Outline platelets.
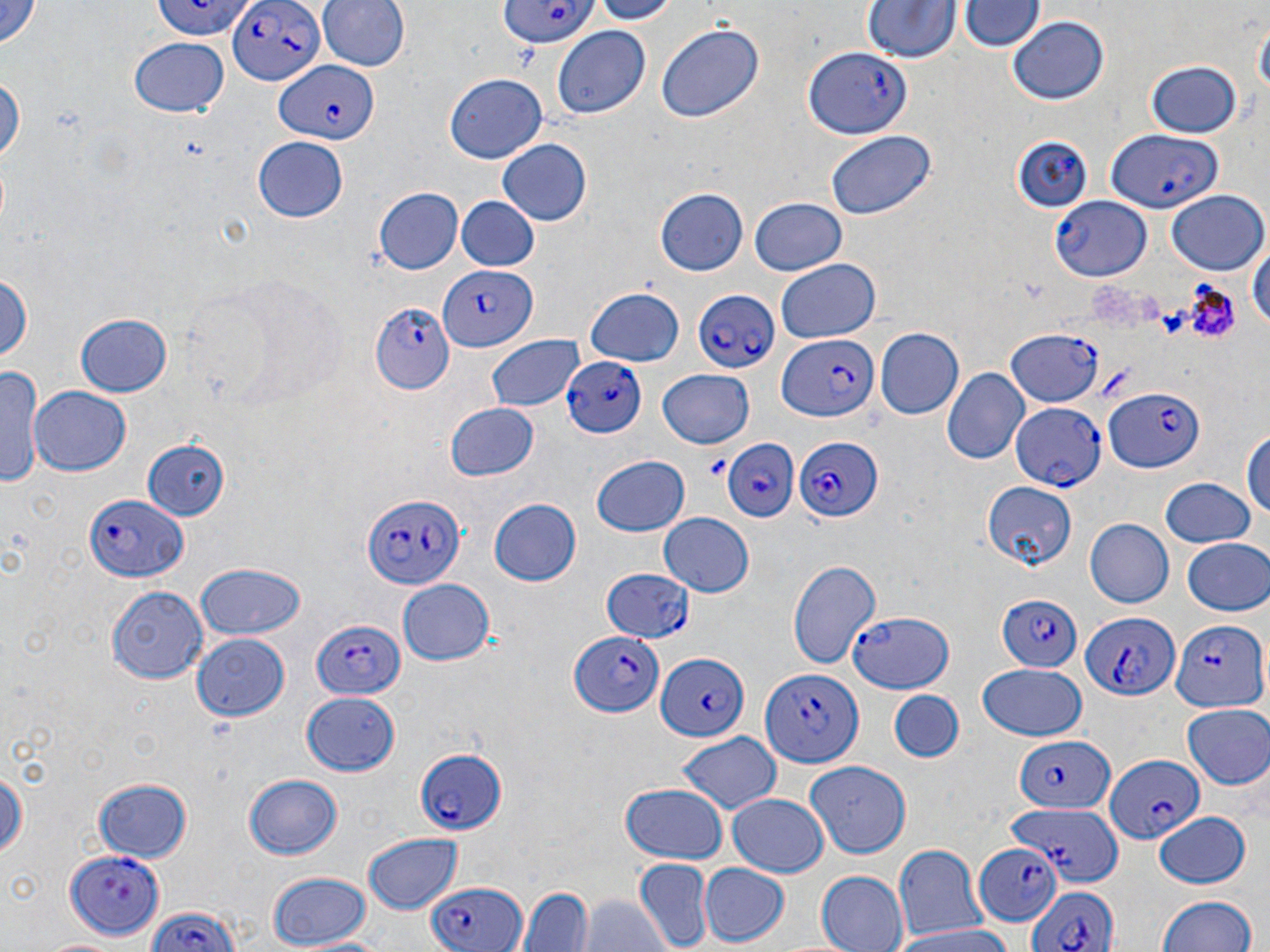
Approximate bounding boxes as [x1, y1, x2, y2] in pixels.
Platelets: [702, 452, 731, 481].

Plasmodium falciparum-infected red blood cell locations: [153, 0, 250, 40], [227, 0, 324, 88], [491, 3, 601, 47], [804, 44, 912, 140], [271, 64, 378, 147], [1108, 130, 1222, 213], [1012, 134, 1091, 214], [1052, 197, 1151, 279], [435, 266, 536, 352], [693, 287, 778, 374], [371, 300, 454, 394], [1008, 328, 1098, 408], [777, 336, 878, 423], [562, 354, 646, 438], [1102, 387, 1204, 474], [1009, 401, 1104, 491], [798, 435, 884, 522], [719, 437, 800, 524], [84, 489, 191, 583], [362, 491, 468, 590], [597, 564, 697, 649], [995, 593, 1083, 672], [849, 608, 955, 693], [1082, 613, 1180, 700], [1167, 618, 1266, 711], [309, 620, 404, 699], [571, 628, 665, 719], [653, 650, 750, 742], [756, 660, 865, 770], [1012, 736, 1115, 812], [415, 747, 508, 833], [1103, 755, 1202, 844], [1012, 795, 1124, 884], [971, 842, 1063, 924], [66, 848, 166, 936], [422, 881, 527, 952], [1027, 884, 1117, 952], [143, 908, 248, 952]. Uninfected red blood cell locations: [0, 0, 46, 46], [317, 0, 407, 74], [585, 0, 681, 24], [863, 1, 960, 64], [962, 1, 1041, 53], [1253, 12, 1268, 107], [1007, 16, 1109, 106], [656, 24, 762, 126], [550, 26, 651, 117], [130, 39, 228, 118], [1144, 61, 1243, 137], [0, 73, 24, 169], [444, 74, 548, 164], [826, 128, 934, 220], [253, 138, 349, 222], [496, 139, 592, 226], [654, 187, 749, 275], [373, 188, 463, 273], [1166, 191, 1267, 273], [455, 196, 541, 273], [747, 197, 848, 276], [1251, 231, 1269, 338], [774, 259, 882, 343], [0, 270, 33, 368], [583, 286, 686, 367], [76, 313, 173, 397], [873, 327, 962, 420], [485, 333, 584, 410], [1, 365, 45, 488], [659, 368, 754, 448], [942, 368, 1030, 466], [31, 386, 133, 478], [446, 402, 540, 482], [1244, 423, 1270, 532], [141, 439, 230, 522], [590, 454, 690, 536], [1159, 479, 1257, 549], [981, 480, 1076, 570], [489, 498, 582, 587], [657, 512, 754, 597], [1086, 517, 1174, 610], [1183, 538, 1270, 616], [788, 557, 882, 673], [195, 561, 306, 639], [395, 579, 495, 666], [105, 585, 208, 681], [192, 633, 289, 721], [978, 664, 1087, 740], [889, 687, 964, 763], [301, 690, 401, 775], [1183, 704, 1270, 788], [675, 730, 783, 814], [0, 761, 26, 865], [803, 761, 913, 858], [242, 774, 344, 861], [93, 775, 194, 861], [617, 782, 729, 864], [727, 794, 829, 878], [1151, 810, 1251, 890], [360, 832, 465, 912], [893, 843, 985, 941], [635, 859, 712, 950], [697, 864, 789, 945], [264, 870, 372, 948], [814, 871, 908, 952], [519, 886, 593, 952], [579, 892, 669, 952], [1156, 893, 1258, 952], [892, 922, 1012, 952], [40, 936, 133, 952]. Slide-level diagnosis: Plasmodium falciparum. Image is 1270×952 pixels. Thin blood smear. Light microscopy. May-Grünwald-Giemsa-stained preparation. One field of a larger specimen. 1000x magnification.